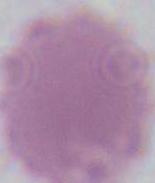

{
  "magnification": "1000x",
  "modality": "photomicrograph",
  "identification": "red blood cell"
}